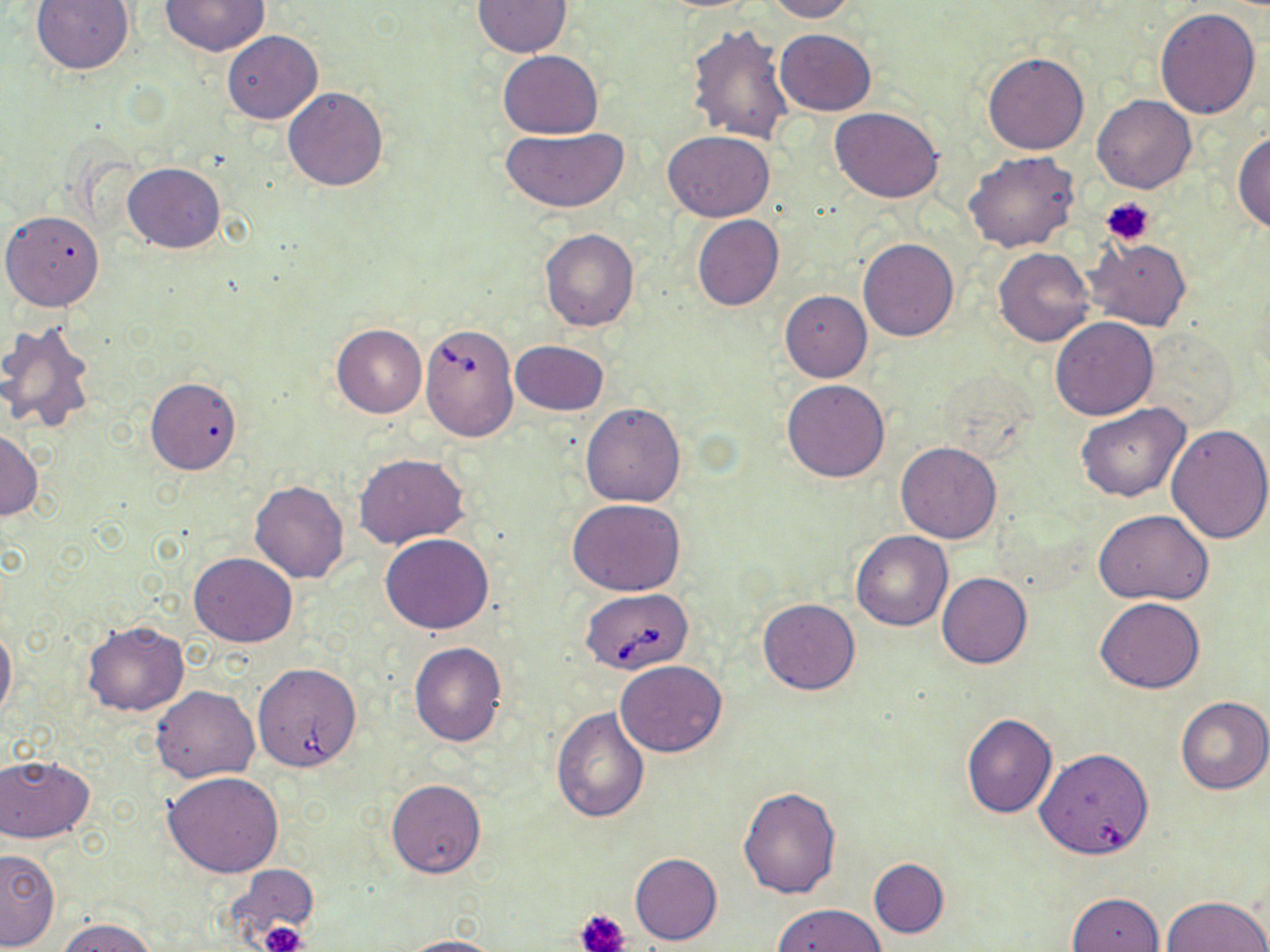
slide-level diagnosis = Babesia divergens
platelet locations = approximate bounding boxes as named x1/y1/x2/y2 corners in pixels: (x1=1103, y1=196, x2=1155, y2=245), (x1=577, y1=907, x2=630, y2=952), (x1=259, y1=921, x2=308, y2=952)
stain = May-Grünwald-Giemsa
preparation = thin blood smear
magnification = 1000x
uninfected red blood cell locations = approximate bounding boxes as named x1/y1/x2/y2 corners in pixels: (x1=30, y1=0, x2=136, y2=75), (x1=160, y1=0, x2=268, y2=55), (x1=764, y1=0, x2=860, y2=22), (x1=472, y1=1, x2=573, y2=57), (x1=1154, y1=7, x2=1261, y2=120), (x1=687, y1=21, x2=795, y2=147), (x1=775, y1=29, x2=876, y2=116), (x1=222, y1=30, x2=322, y2=124), (x1=497, y1=49, x2=604, y2=137), (x1=982, y1=52, x2=1090, y2=154), (x1=282, y1=86, x2=390, y2=191), (x1=1093, y1=94, x2=1196, y2=193), (x1=830, y1=107, x2=943, y2=202), (x1=501, y1=127, x2=629, y2=213), (x1=662, y1=131, x2=774, y2=222), (x1=1234, y1=131, x2=1270, y2=235), (x1=965, y1=151, x2=1080, y2=253), (x1=124, y1=162, x2=225, y2=254), (x1=2, y1=210, x2=104, y2=310), (x1=692, y1=214, x2=784, y2=310), (x1=539, y1=229, x2=640, y2=332), (x1=858, y1=238, x2=958, y2=342), (x1=1083, y1=238, x2=1191, y2=330), (x1=993, y1=247, x2=1095, y2=347), (x1=780, y1=290, x2=872, y2=382), (x1=1051, y1=317, x2=1158, y2=419), (x1=0, y1=322, x2=97, y2=433), (x1=331, y1=324, x2=427, y2=417), (x1=510, y1=340, x2=609, y2=415), (x1=145, y1=376, x2=242, y2=474), (x1=781, y1=379, x2=890, y2=483), (x1=580, y1=402, x2=685, y2=507), (x1=1075, y1=402, x2=1190, y2=503), (x1=1165, y1=424, x2=1270, y2=544), (x1=0, y1=428, x2=43, y2=522), (x1=895, y1=441, x2=1002, y2=543), (x1=354, y1=454, x2=468, y2=550), (x1=250, y1=481, x2=349, y2=583), (x1=567, y1=498, x2=686, y2=596), (x1=1093, y1=510, x2=1214, y2=606), (x1=850, y1=530, x2=952, y2=630), (x1=380, y1=533, x2=494, y2=634), (x1=189, y1=552, x2=296, y2=646), (x1=936, y1=573, x2=1031, y2=669), (x1=1095, y1=596, x2=1205, y2=693), (x1=757, y1=598, x2=861, y2=694), (x1=0, y1=622, x2=16, y2=724), (x1=84, y1=622, x2=189, y2=716), (x1=408, y1=643, x2=506, y2=745), (x1=615, y1=660, x2=727, y2=757), (x1=151, y1=684, x2=260, y2=782), (x1=1176, y1=696, x2=1270, y2=795), (x1=551, y1=707, x2=649, y2=823), (x1=961, y1=713, x2=1058, y2=818), (x1=1035, y1=747, x2=1154, y2=860), (x1=0, y1=754, x2=94, y2=843), (x1=163, y1=772, x2=283, y2=877), (x1=387, y1=779, x2=486, y2=878), (x1=738, y1=786, x2=840, y2=898), (x1=0, y1=849, x2=60, y2=950), (x1=630, y1=852, x2=722, y2=945), (x1=869, y1=858, x2=948, y2=938), (x1=231, y1=867, x2=318, y2=942), (x1=1065, y1=891, x2=1165, y2=952), (x1=1162, y1=897, x2=1269, y2=952), (x1=774, y1=904, x2=885, y2=952), (x1=57, y1=917, x2=156, y2=952), (x1=394, y1=936, x2=509, y2=952)
field of view = single
image size = 1270×952 pixels
modality = light microscopy
Babesia divergens-infected red blood cell locations = approximate bounding boxes as named x1/y1/x2/y2 corners in pixels: (x1=420, y1=322, x2=518, y2=441), (x1=581, y1=588, x2=693, y2=673), (x1=248, y1=662, x2=365, y2=775)